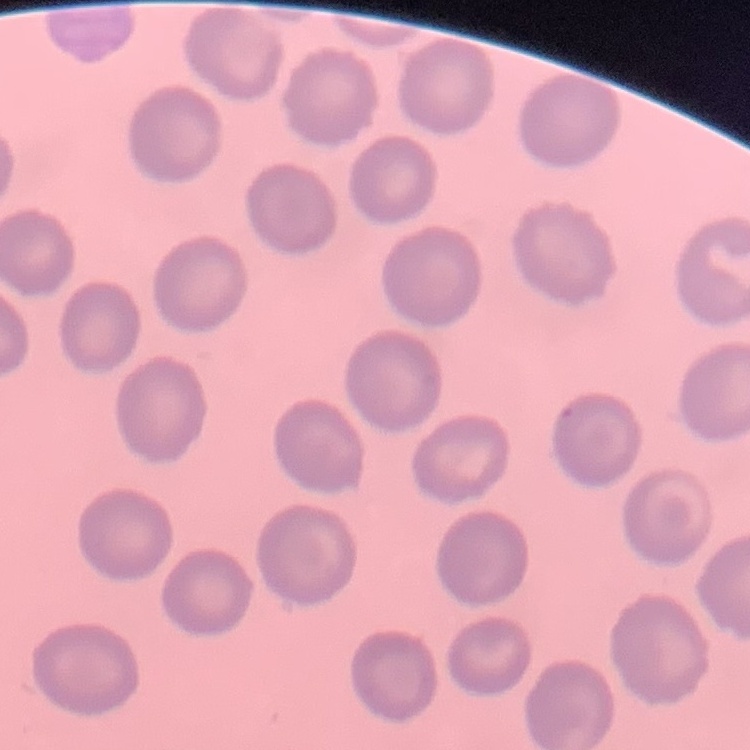

Summary:
  - Erythrocyte morphology: no rouleaux formation
  - Image type: one tile cut from a larger photomicrograph
  - Preparation: thin peripheral smear
  - Stain: Field's or Giemsa